Locate every leukocyte (white blood cell).
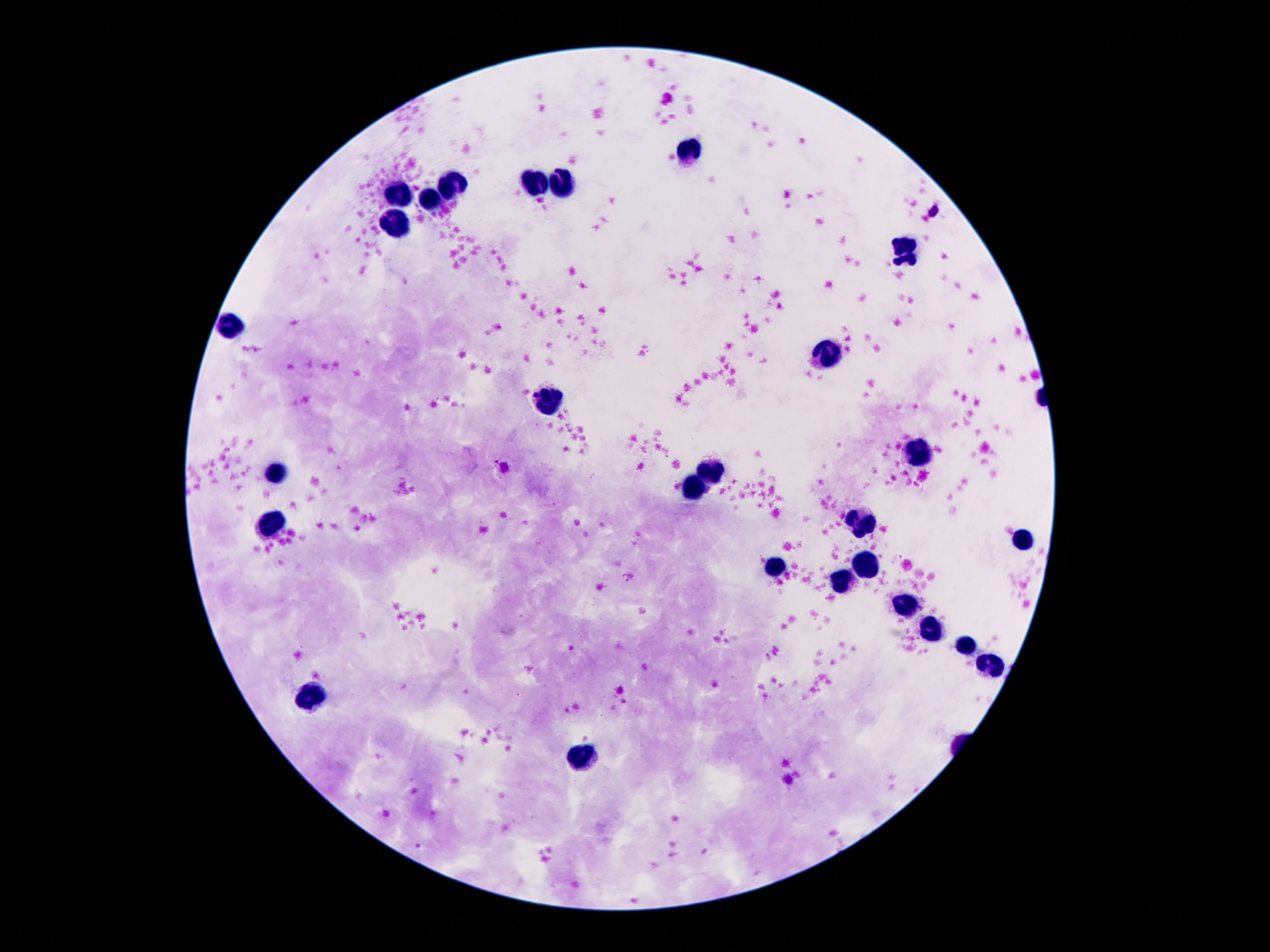

Approximate object centers, in pixels from the top-left corner.
Leukocytes: (x=691, y=148), (x=535, y=182), (x=570, y=183), (x=453, y=187), (x=396, y=194), (x=431, y=200), (x=396, y=224), (x=904, y=250), (x=234, y=326), (x=828, y=354), (x=550, y=402), (x=920, y=456), (x=711, y=470), (x=277, y=472), (x=695, y=491), (x=861, y=523), (x=277, y=526), (x=1023, y=540), (x=865, y=566), (x=773, y=568), (x=839, y=585), (x=906, y=601), (x=929, y=628), (x=968, y=646), (x=988, y=661), (x=316, y=695), (x=580, y=759).

Summary:
  - Preparation: thick peripheral-blood smear
  - Magnification: 100x
  - Image size: 1270×952 pixels
  - Stain: Giemsa
  - Patient malaria status: not infected
  - Capture: smartphone camera through the microscope eyepiece
  - Field of view: single